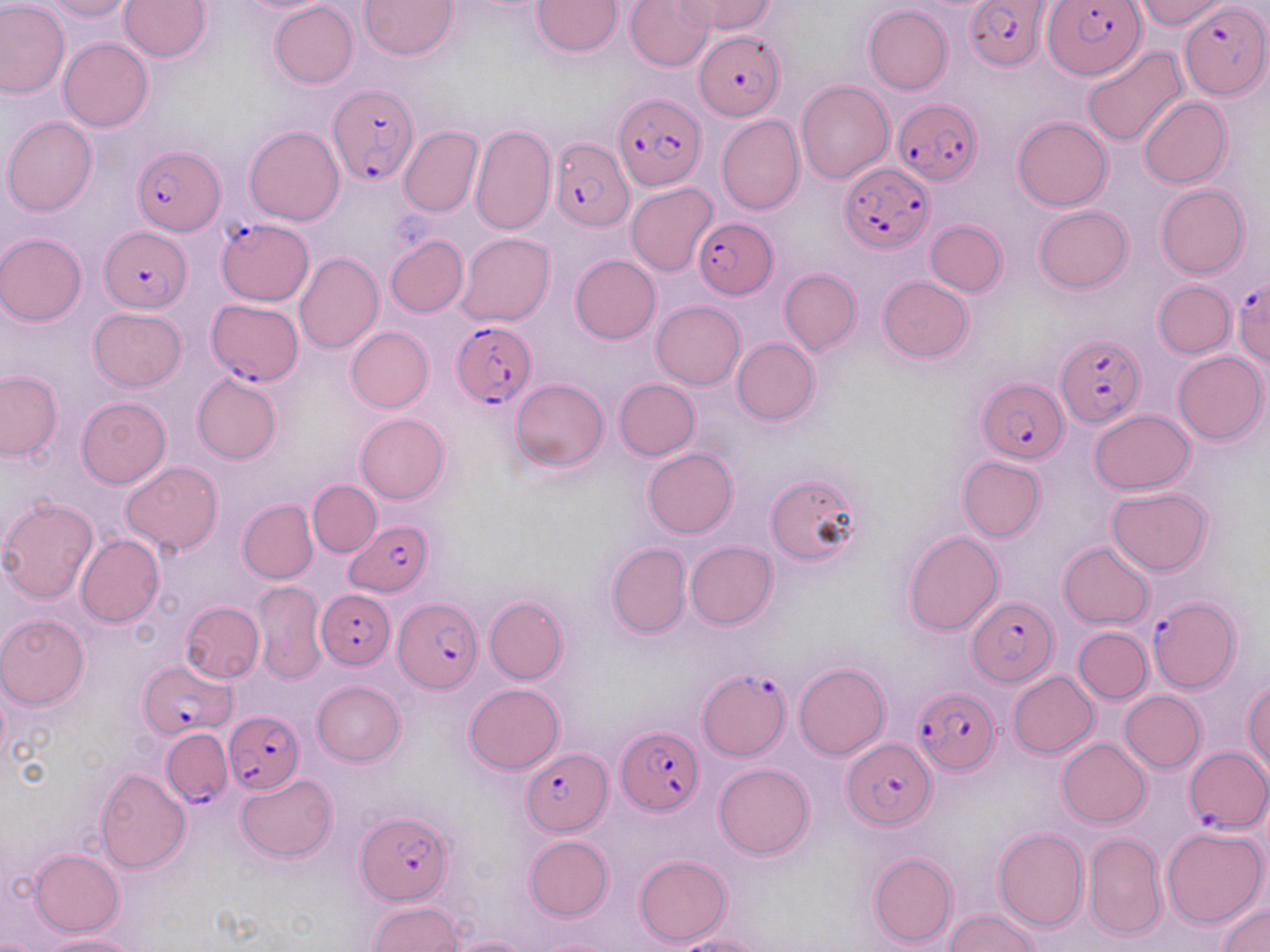

slide_level_diagnosis: Plasmodium falciparum
magnification: 1000x
plasmodium_falciparum_infected_red_blood_cell_locations_subset: 'approximate bounding boxes as (x1,y1)-(x2,y2) corner pairs in pixels: (966,0)-(1049,71), (1044,0)-(1146,80), (1181,3)-(1267,99), (695,32)-(785,120), (329,84)-(418,185), (613,94)-(705,193), (893,98)-(981,187), (549,134)-(633,230), (132,144)-(222,236), (839,163)-(933,253), (694,218)-(778,299), (217,220)-(315,304), (100,226)-(192,313), (1232,276)-(1270,368), (209,297)-(303,384), (451,320)-(535,409), (1056,333)-(1145,430), (978,377)-(1066,463), (346,518)-(435,596), (316,589)-(396,669), (1149,593)-(1239,693), (394,598)-(480,692), (968,599)-(1056,686), (140,661)-(230,739), (699,671)-(788,759), (912,686)-(998,775), (222,709)-(303,793), (618,728)-(703,816), (163,729)-(235,807), (843,739)-(936,828), (1185,745)-(1269,833), (524,750)-(611,834), (356,812)-(454,905)'
image_size: 1270×952 pixels
stain: May-Grünwald-Giemsa
modality: optical microscopy
field_of_view: single
preparation: thin blood film
uninfected_red_blood_cell_locations_subset: 'approximate bounding boxes as (x1,y1)-(x2,y2) corner pairs in pixels: (0,0)-(71,99), (42,0)-(135,20), (119,0)-(211,61), (360,0)-(457,60), (534,0)-(621,56), (626,0)-(715,71), (674,0)-(775,33), (1134,0)-(1229,28), (270,2)-(358,89), (863,4)-(952,95), (59,38)-(153,131), (1083,47)-(1189,150), (796,80)-(894,183), (1138,96)-(1231,188), (717,115)-(804,215), (2,116)-(98,215), (1012,116)-(1113,211), (245,125)-(344,226), (399,126)-(482,217), (626,183)-(717,277), (1156,185)-(1250,279), (1034,206)-(1132,293), (926,220)-(1007,295), (0,233)-(86,325), (456,234)-(554,327), (385,235)-(468,317), (295,252)-(383,355), (570,254)-(661,344), (779,269)-(861,354), (877,277)-(973,363), (1153,280)-(1236,358), (652,301)-(745,389), (89,308)-(186,391), (346,326)-(433,412), (732,337)-(820,424), (1172,351)-(1266,444), (0,371)-(63,462), (192,371)-(282,464), (510,378)-(608,471), (613,378)-(700,461), (76,396)-(170,486), (1088,409)-(1196,494), (355,412)-(449,503), (643,447)-(737,537), (956,456)-(1047,542), (122,462)-(222,554), (764,473)-(862,566), (308,481)-(381,556), (1107,488)-(1214,575), (0,497)-(99,605), (238,499)-(318,583), (902,530)-(1004,636), (75,534)-(164,628), (685,540)-(777,629), (1059,541)-(1154,629), (606,543)-(690,638), (254,580)-(327,683), (485,596)-(568,684), (181,601)-(265,683), (0,615)-(90,709), (1074,627)-(1152,703), (794,662)-(891,760), (1009,671)-(1098,758), (1244,680)-(1270,775), (312,681)-(405,765), (466,682)-(564,772), (1120,691)-(1206,772), (1058,738)-(1152,828), (714,763)-(814,859), (95,769)-(191,873), (236,775)-(335,862), (993,826)-(1088,933), (1161,826)-(1268,929), (1083,831)-(1166,941), (524,836)-(613,921), (29,849)-(123,936), (868,852)-(958,949), (635,855)-(732,946), (369,902)-(464,952), (1219,903)-(1270,952), (944,910)-(1041,952), (39,934)-(138,952), (674,935)-(763,952), (447,936)-(533,952), (536,937)-(624,952)'